Identify the parasite.
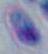
This is Toxoplasma gondii.

modality = photomicrograph
magnification = 1000x